Assess the morphology of the erythrocytes.
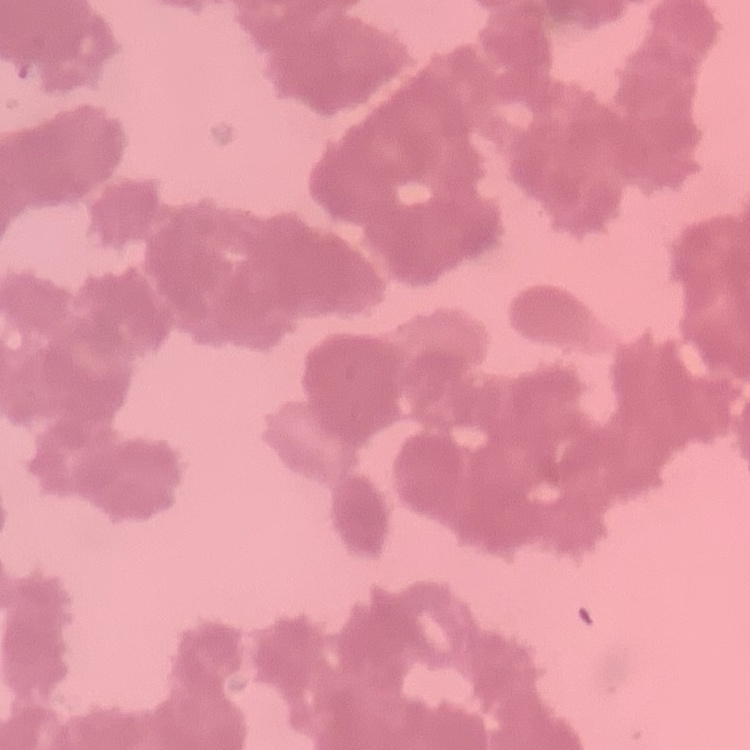

They show rouleaux formation.

Summary:
  - Stain: Field's or Giemsa
  - Image type: one tile cut from a larger photomicrograph
  - Preparation: thin peripheral smear